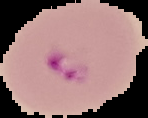 From a thin blood film. Image is 148×118 pixels. Result: malaria parasites detected. Segmented cell region on a black background.